Describe the morphology of the red blood cells.
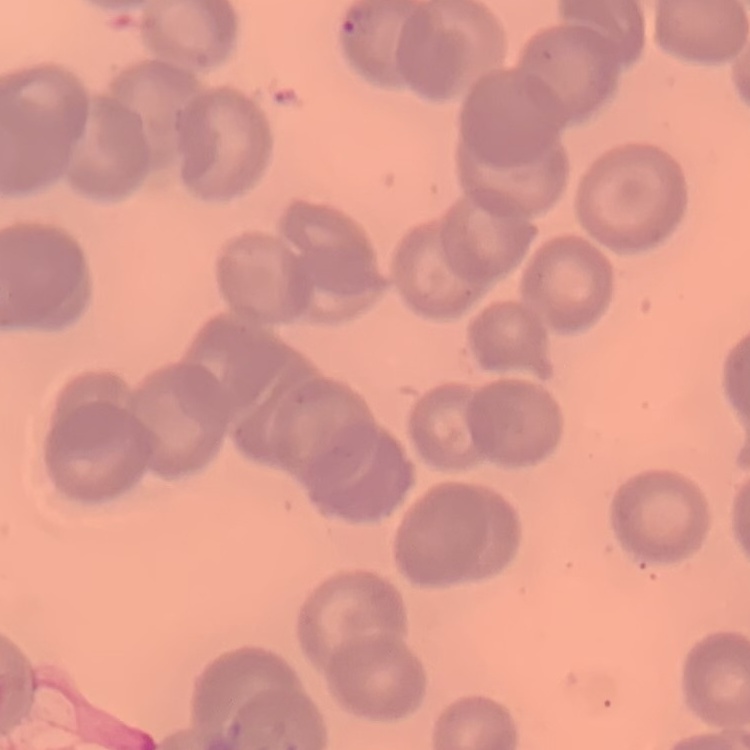

No rouleaux formation.

Thin peripheral smear. Square crop of a larger photomicrograph. Stained with either Field's or Giemsa.